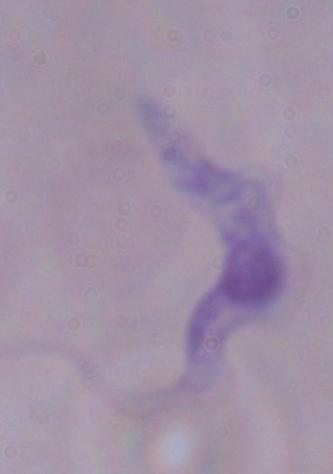

Micrograph. 1000x magnification. A trypanosome is shown.